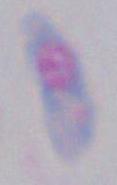

Summary:
  - Identification: Toxoplasma gondii
  - Modality: photomicrograph
  - Magnification: 1000x